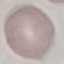 Malaria status: uninfected. Giemsa-stained preparation. Cell patch, automatically extracted from a larger field of view and resized to 64 × 64 pixels. Acquired by smartphone through the microscope eyepiece. Thin smear of blood.